Assess this cell for malaria.
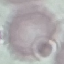

Uninfected.

preparation: thin blood smear
capture: smartphone through the microscope eyepiece
stain: Giemsa
image_type: automatically extracted cell patch, resized to 64 × 64 pixels